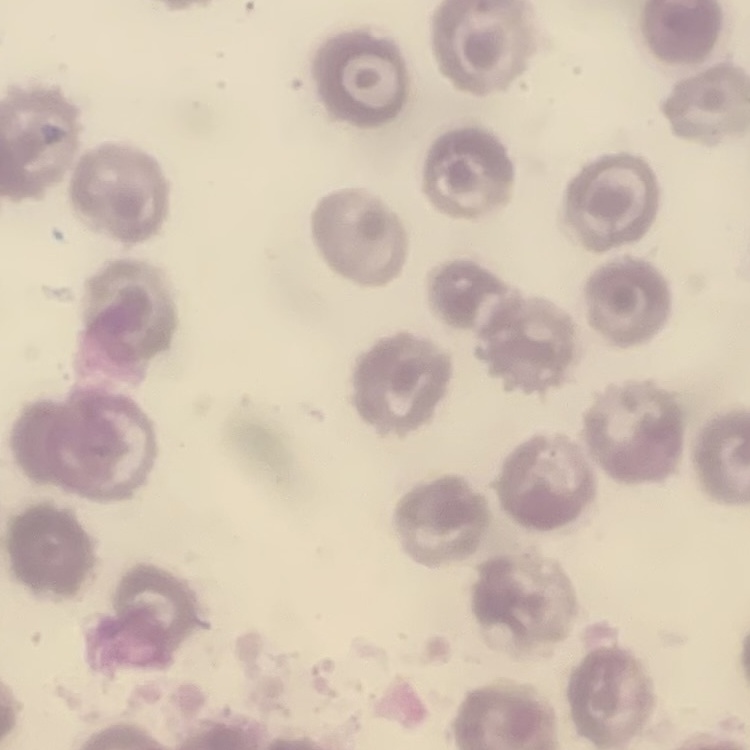

red_blood_cell_morphology: no rouleaux formation
preparation: thin blood smear
image_type: square crop of a larger photomicrograph
stain: Field's or Giemsa